State the blood parasite species.
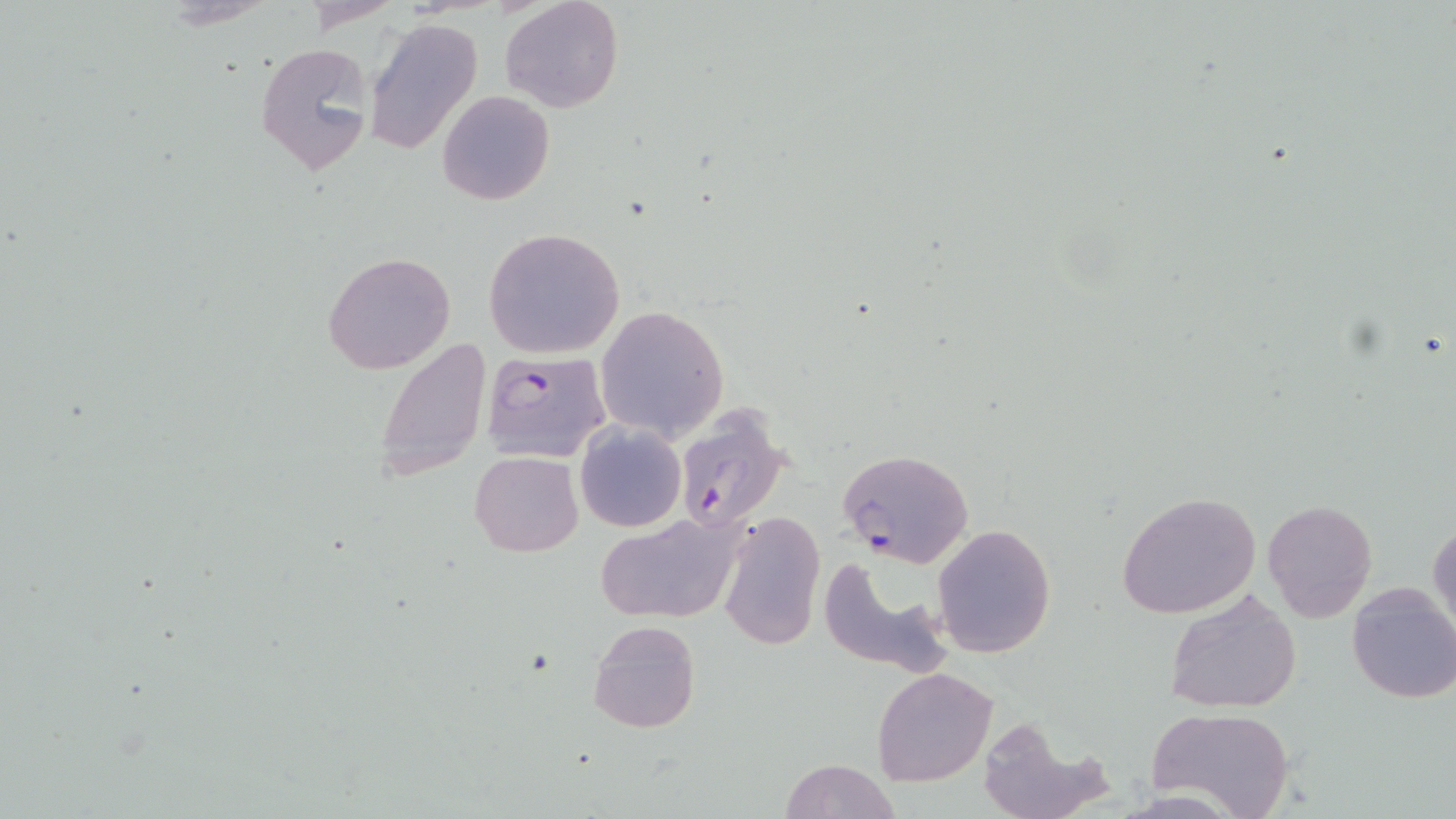

Plasmodium falciparum.

Summary:
  - Coordinate format: approximate bounding boxes as named x1/y1/x2/y2 corners in pixels
  - Uninfected red blood cell locations: (x1=501, y1=0, x2=623, y2=113), (x1=364, y1=17, x2=484, y2=155), (x1=253, y1=39, x2=377, y2=174), (x1=437, y1=90, x2=554, y2=206), (x1=483, y1=228, x2=625, y2=357), (x1=322, y1=250, x2=457, y2=375), (x1=594, y1=305, x2=730, y2=442), (x1=376, y1=337, x2=489, y2=482), (x1=575, y1=422, x2=685, y2=532), (x1=468, y1=450, x2=584, y2=557), (x1=1116, y1=491, x2=1263, y2=619), (x1=1262, y1=499, x2=1378, y2=621), (x1=719, y1=509, x2=824, y2=650), (x1=594, y1=518, x2=746, y2=623), (x1=1427, y1=518, x2=1455, y2=640), (x1=931, y1=523, x2=1057, y2=659), (x1=815, y1=553, x2=953, y2=675), (x1=1346, y1=582, x2=1456, y2=704), (x1=1164, y1=587, x2=1302, y2=715), (x1=588, y1=620, x2=700, y2=734), (x1=871, y1=667, x2=998, y2=786), (x1=1147, y1=708, x2=1294, y2=819), (x1=973, y1=715, x2=1106, y2=819), (x1=780, y1=758, x2=901, y2=819)
  - Plasmodium falciparum-infected red blood cell locations: (x1=481, y1=349, x2=611, y2=463), (x1=673, y1=404, x2=792, y2=536), (x1=836, y1=448, x2=974, y2=569)
  - Stain: May-Grünwald-Giemsa
  - Modality: light microscopy
  - Magnification: 1000x
  - Field of view: one of a larger specimen
  - Preparation: thin blood film
  - Image size: 1456×819 pixels